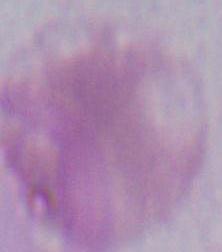
Summary:
  - Modality: micrograph
  - Identification: erythrocyte
  - Magnification: 1000x